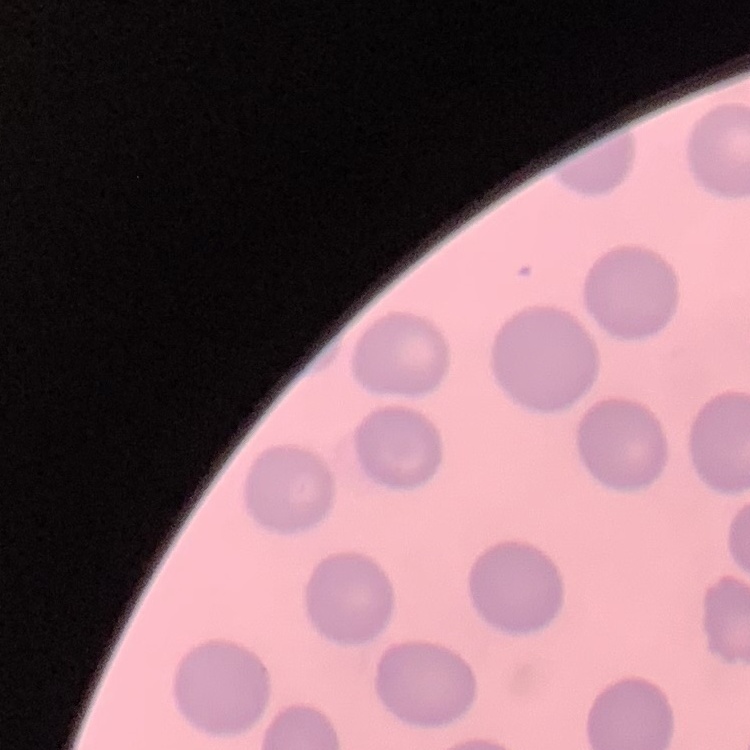
erythrocyte_morphology: no rouleaux formation
image_type: one tile cut from a larger photomicrograph
stain: Field's or Giemsa
preparation: thin peripheral smear